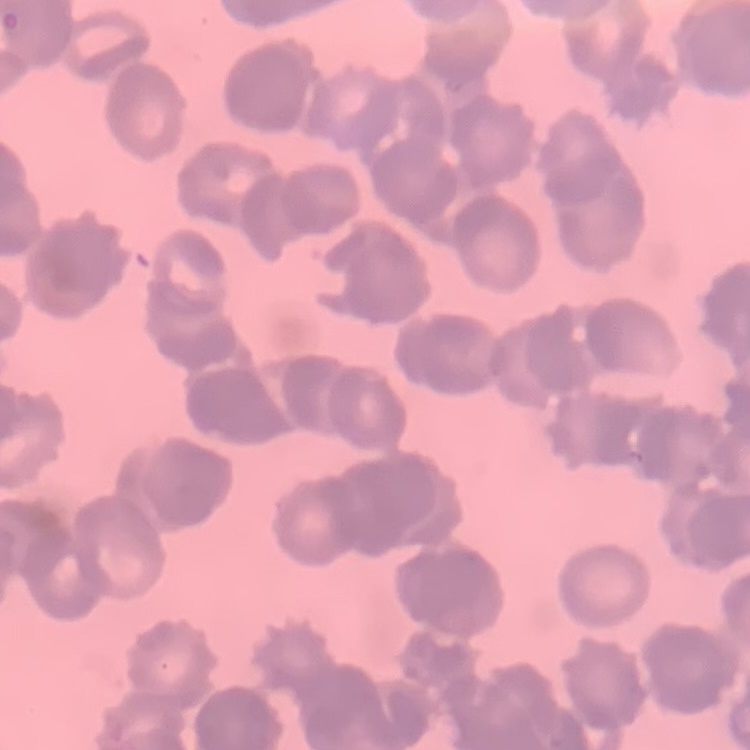

Summary:
  - Erythrocyte morphology: rouleaux formation
  - Stain: Field's or Giemsa
  - Image type: square crop of a larger photomicrograph
  - Preparation: thin peripheral smear